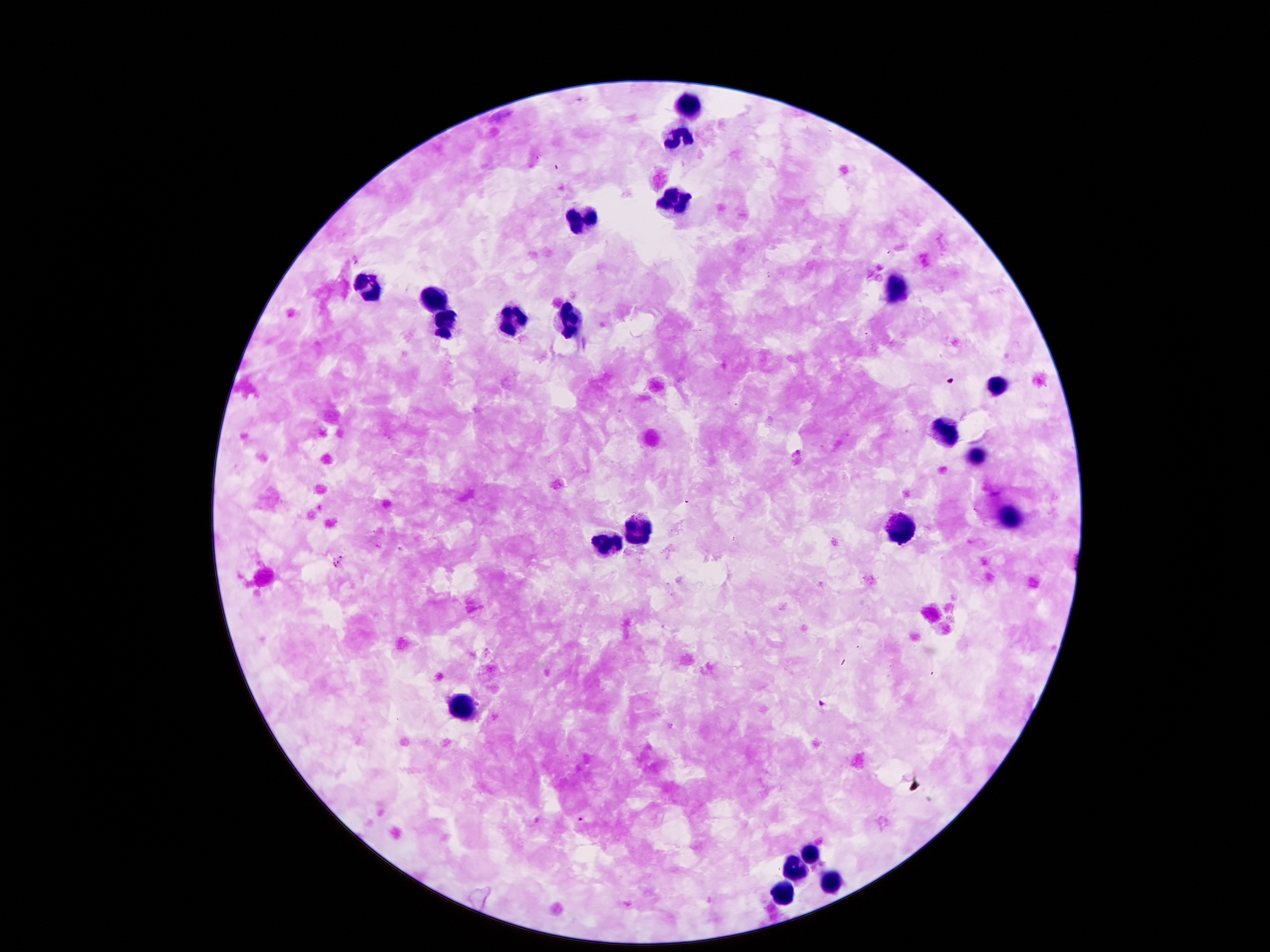
Approximate centers as (x, y) in pixels. Plasmodium parasite locations: (557, 166), (888, 253), (769, 275), (698, 330), (866, 334), (951, 381), (686, 502), (338, 562), (823, 704), (581, 820). Leukocyte locations: (688, 106), (679, 137), (675, 197), (580, 221), (365, 285), (892, 290), (434, 303), (516, 320), (446, 322), (571, 322), (994, 384), (948, 432), (976, 455), (1011, 520), (903, 529), (638, 531), (606, 544), (460, 705), (811, 852), (800, 865), (832, 886), (787, 893). Photographed through the microscope eyepiece with a smartphone camera. Giemsa stain. 100x magnification. Single field of view. Image is 1270×952 pixels. Patient malaria status: positive for Plasmodium falciparum. Thick blood smear.